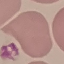
Result: no malaria parasites seen. Giemsa-stained preparation. Automatically extracted cell patch, resized to 64 × 64 pixels. Thin blood smear. Acquired by smartphone through the microscope eyepiece.